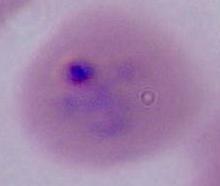

Summary:
  - Modality: micrograph
  - Identification: Plasmodium
  - Magnification: 400x or 1000x